Outline platelets.
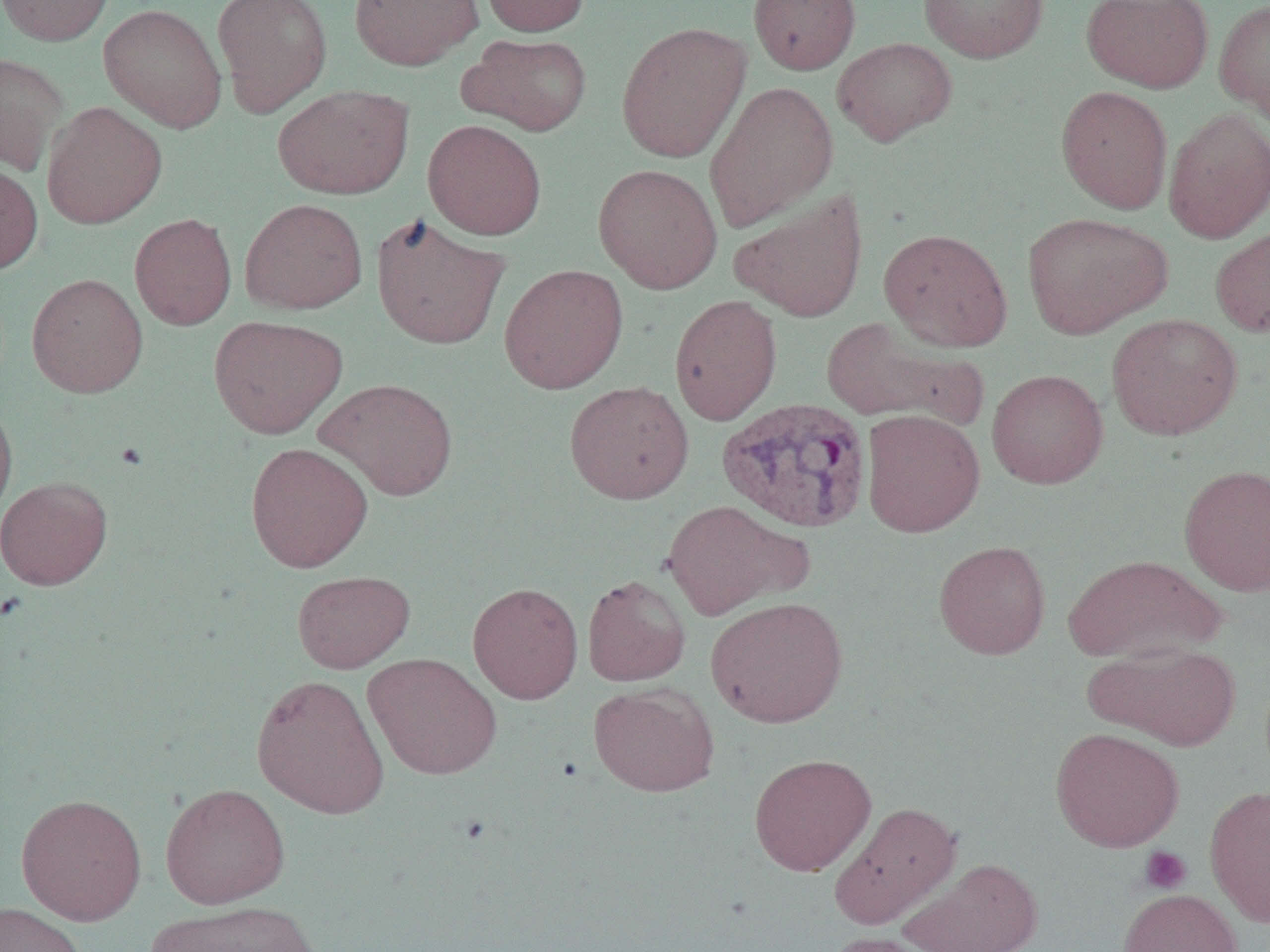

Approximate bounding boxes as (x1,y1)-(x2,y2) corner pairs in pixels.
Platelets: (1138,846)-(1192,895).

Summary:
  - Plasmodium vivax-infected red blood cell locations: (717,396)-(872,533)
  - Uninfected red blood cell locations: (0,0)-(114,46), (211,0)-(333,117), (349,0)-(483,70), (480,0)-(590,36), (748,0)-(861,75), (918,0)-(1049,63), (1080,0)-(1213,93), (1214,0)-(1270,127), (98,3)-(228,133), (615,22)-(751,163), (458,33)-(593,136), (832,37)-(957,146), (0,53)-(69,175), (704,80)-(839,233), (272,84)-(414,200), (1055,85)-(1173,213), (42,102)-(167,229), (1163,108)-(1270,243), (423,119)-(546,240), (0,161)-(43,274), (592,163)-(723,294), (729,188)-(869,322), (239,198)-(368,314), (1022,211)-(1171,339), (129,213)-(237,330), (371,214)-(510,350), (1210,224)-(1270,338), (878,227)-(1013,351), (499,264)-(628,394), (27,273)-(148,398), (669,295)-(782,425), (1106,313)-(1242,441), (208,314)-(348,438), (820,316)-(985,430), (986,368)-(1108,489), (316,377)-(458,501), (564,381)-(694,504), (0,399)-(17,523), (861,409)-(985,538), (245,442)-(373,573), (1178,463)-(1270,596), (0,475)-(113,590), (661,499)-(811,621), (934,540)-(1051,659), (1064,554)-(1225,664), (292,570)-(414,673), (582,574)-(690,687), (467,582)-(583,704), (705,596)-(848,728), (1085,642)-(1241,750), (363,653)-(502,780), (251,674)-(390,819), (588,682)-(720,796), (1049,727)-(1184,852), (749,753)-(877,875), (160,783)-(290,908), (1204,784)-(1270,927), (15,793)-(148,925), (829,800)-(962,929), (901,858)-(1044,952), (1118,888)-(1242,952), (148,901)-(320,952), (0,902)-(86,952), (822,931)-(946,952)
  - Slide-level diagnosis: Plasmodium vivax
  - Magnification: 1000x
  - Modality: optical microscopy
  - Field of view: single
  - Preparation: thin blood film
  - Image size: 1270×952 pixels